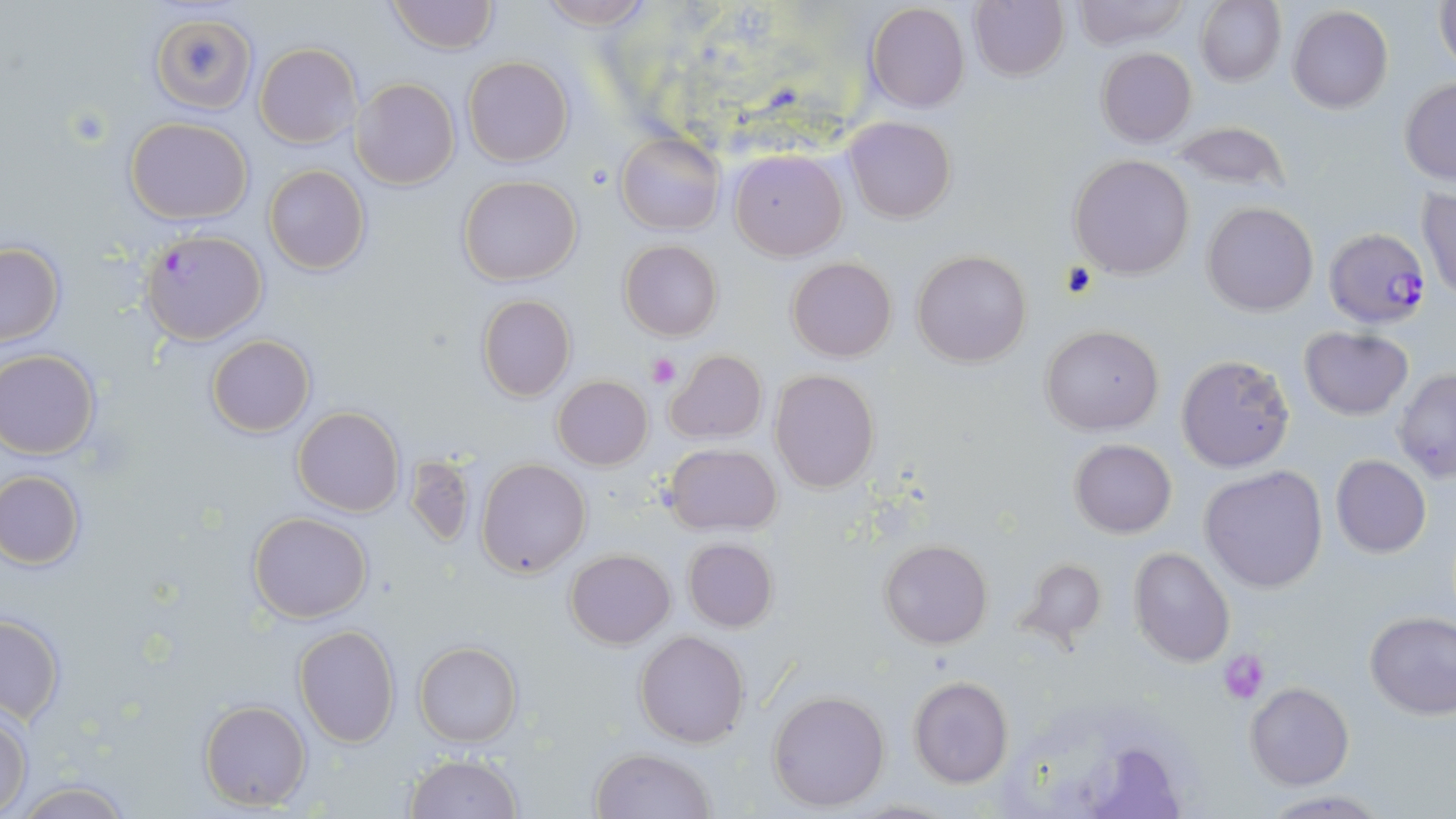 Approximate bounding boxes as named x1/y1/x2/y2 corners in pixels. Uninfected red blood cell locations: (x1=387, y1=0, x2=497, y2=54), (x1=533, y1=0, x2=658, y2=29), (x1=1195, y1=0, x2=1286, y2=87), (x1=1432, y1=0, x2=1455, y2=74), (x1=969, y1=1, x2=1069, y2=81), (x1=1069, y1=1, x2=1192, y2=49), (x1=864, y1=2, x2=971, y2=114), (x1=1288, y1=6, x2=1394, y2=114), (x1=151, y1=10, x2=254, y2=111), (x1=254, y1=43, x2=360, y2=149), (x1=1096, y1=47, x2=1197, y2=147), (x1=463, y1=56, x2=573, y2=167), (x1=352, y1=77, x2=459, y2=190), (x1=1399, y1=79, x2=1456, y2=184), (x1=124, y1=117, x2=254, y2=222), (x1=845, y1=117, x2=957, y2=223), (x1=1172, y1=120, x2=1291, y2=196), (x1=616, y1=133, x2=724, y2=235), (x1=729, y1=149, x2=847, y2=259), (x1=1069, y1=154, x2=1195, y2=279), (x1=264, y1=165, x2=370, y2=276), (x1=458, y1=175, x2=581, y2=286), (x1=1417, y1=188, x2=1455, y2=299), (x1=1203, y1=202, x2=1318, y2=316), (x1=619, y1=240, x2=723, y2=341), (x1=0, y1=243, x2=63, y2=346), (x1=911, y1=249, x2=1033, y2=366), (x1=787, y1=256, x2=896, y2=363), (x1=477, y1=295, x2=576, y2=402), (x1=1040, y1=324, x2=1164, y2=435), (x1=1299, y1=327, x2=1414, y2=420), (x1=207, y1=335, x2=315, y2=438), (x1=665, y1=349, x2=767, y2=444), (x1=0, y1=350, x2=101, y2=458), (x1=1176, y1=353, x2=1296, y2=473), (x1=1392, y1=367, x2=1456, y2=482), (x1=770, y1=369, x2=880, y2=493), (x1=553, y1=376, x2=653, y2=470), (x1=293, y1=406, x2=405, y2=517), (x1=1070, y1=439, x2=1177, y2=537), (x1=663, y1=443, x2=782, y2=535), (x1=404, y1=455, x2=477, y2=549), (x1=1331, y1=456, x2=1431, y2=557), (x1=476, y1=459, x2=592, y2=579), (x1=1200, y1=465, x2=1329, y2=592), (x1=0, y1=471, x2=86, y2=569), (x1=247, y1=512, x2=372, y2=623), (x1=682, y1=538, x2=779, y2=633), (x1=880, y1=539, x2=993, y2=650), (x1=1127, y1=547, x2=1235, y2=667), (x1=565, y1=548, x2=675, y2=649), (x1=1014, y1=557, x2=1106, y2=648), (x1=1365, y1=612, x2=1456, y2=719), (x1=0, y1=614, x2=65, y2=723), (x1=294, y1=625, x2=401, y2=748), (x1=635, y1=630, x2=749, y2=748), (x1=414, y1=642, x2=522, y2=747), (x1=907, y1=677, x2=1014, y2=788), (x1=1245, y1=682, x2=1352, y2=789), (x1=768, y1=689, x2=891, y2=813), (x1=199, y1=699, x2=313, y2=811), (x1=0, y1=706, x2=32, y2=815), (x1=590, y1=748, x2=717, y2=819), (x1=402, y1=752, x2=522, y2=818), (x1=3, y1=779, x2=142, y2=818). Plasmodium falciparum-infected red blood cell locations: (x1=1323, y1=227, x2=1431, y2=328), (x1=139, y1=229, x2=268, y2=345). Platelet locations: (x1=647, y1=352, x2=681, y2=388), (x1=1218, y1=649, x2=1270, y2=701). Slide-level diagnosis: Plasmodium falciparum. May-Grünwald-Giemsa stain. 1000x magnification. Optical microscopy. One field of a larger specimen. Thin blood film. Image is 1456×819 pixels.